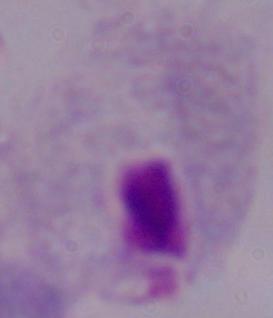

Summary:
  - Magnification: 1000x
  - Identification: trichomonad
  - Modality: photomicrograph